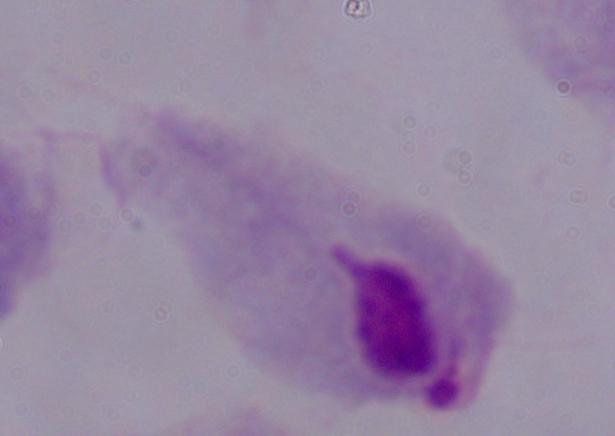

magnification: 1000x
identification: trichomonad
modality: micrograph